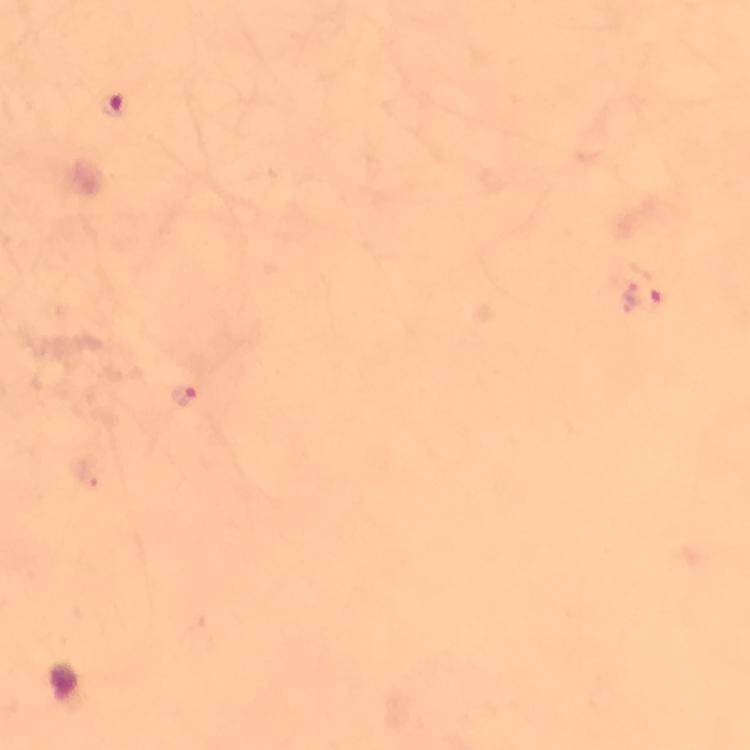

Approximate centers as (x, y) in pixels. Plasmodium parasite locations: (111, 105), (644, 297), (183, 394). Image is 750×750 pixels. Giemsa-stained preparation. From a malaria diagnostic workup. Thick smear. At 100x magnification. Photographed through the microscope with a smartphone camera. Cropped region of a single field of view. Immersion oil applied.